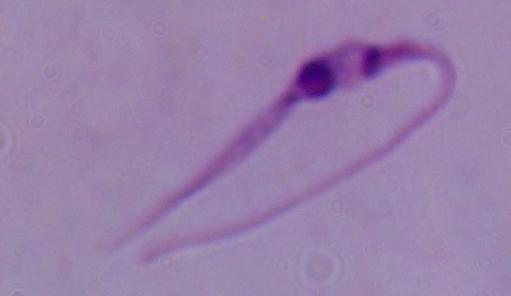
magnification = 1000x
modality = photomicrograph
identification = Leishmania